State which parasite is depicted.
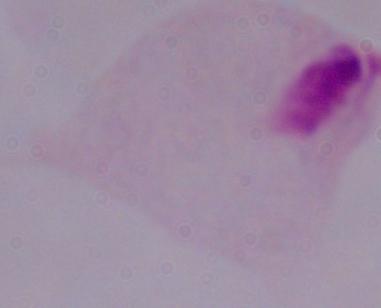
This is a trichomonad.

Photomicrograph. Captured at 1000x magnification.